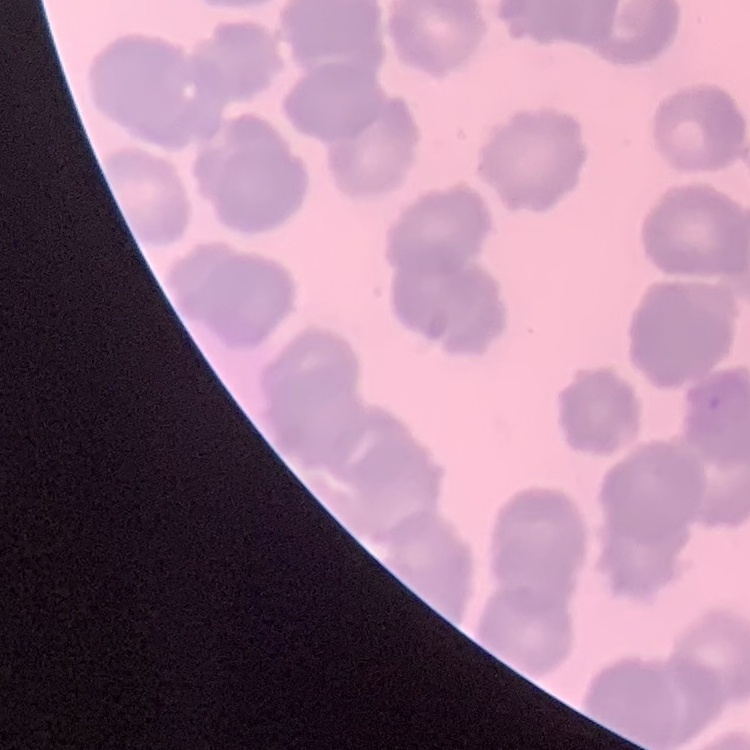 The erythrocytes show rouleaux formation. One tile cut from a larger photomicrograph. Field's or Giemsa stain. Thin blood smear.